Comment on the morphology of the erythrocytes.
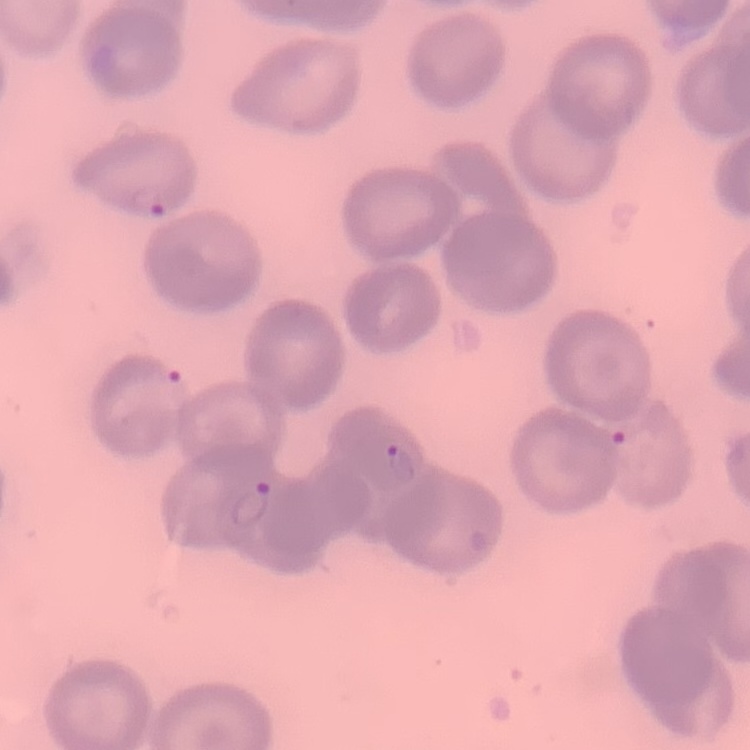
They show no rouleaux formation.

image_type: square crop of a larger photomicrograph
stain: Field's or Giemsa
preparation: thin blood smear